Mark where platelets are.
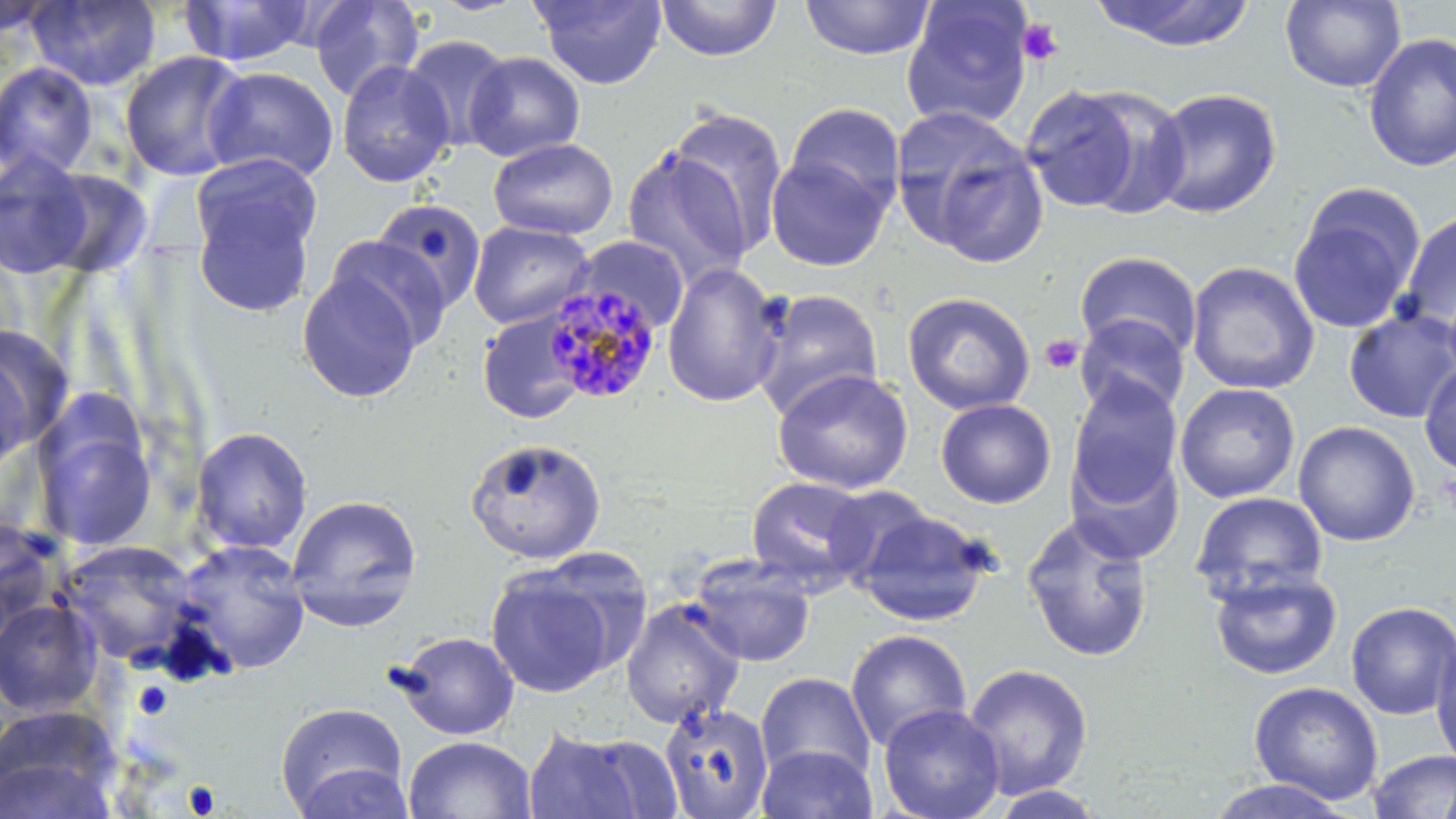

Approximate bounding boxes as (x1, y1, x2, y2) in pixels.
Platelets: (1017, 18, 1064, 66), (1039, 333, 1085, 375), (133, 681, 173, 720), (183, 781, 221, 817).

slide-level diagnosis = Plasmodium malariae
image size = 1456×819 pixels
uninfected red blood cell locations = approximate bounding boxes as (x1, y1, x2, y2) in pixels: (28, 0, 162, 92), (308, 0, 425, 102), (532, 0, 667, 90), (655, 0, 782, 62), (800, 0, 935, 60), (1091, 0, 1256, 51), (1280, 0, 1406, 93), (901, 1, 1035, 130), (0, 2, 56, 39), (178, 2, 315, 68), (1363, 32, 1456, 173), (402, 35, 514, 152), (119, 51, 252, 181), (463, 51, 585, 162), (336, 59, 455, 187), (0, 61, 99, 180), (203, 66, 340, 183), (1020, 85, 1157, 214), (1146, 87, 1282, 219), (783, 101, 907, 221), (890, 105, 1048, 266), (665, 106, 789, 257), (488, 137, 619, 240), (621, 146, 754, 288), (0, 150, 96, 279), (765, 153, 892, 271), (189, 160, 322, 316), (38, 168, 154, 278), (1289, 183, 1425, 335), (370, 198, 487, 314), (1399, 211, 1456, 334), (468, 220, 594, 330), (324, 235, 453, 352), (567, 235, 690, 336), (1074, 251, 1203, 363), (1185, 260, 1321, 395), (662, 262, 786, 407), (296, 268, 424, 403), (749, 288, 885, 420), (902, 291, 1036, 415), (1343, 308, 1456, 423), (477, 311, 588, 424), (1075, 314, 1190, 419), (0, 325, 64, 463), (0, 347, 35, 482), (1418, 360, 1456, 476), (772, 368, 914, 495), (1067, 376, 1182, 508), (1174, 382, 1301, 504), (935, 398, 1057, 508), (31, 411, 160, 551), (1293, 420, 1421, 546), (189, 425, 313, 555), (465, 437, 607, 563), (1066, 446, 1185, 566), (744, 475, 873, 594), (821, 483, 937, 591), (1189, 491, 1328, 605), (286, 494, 423, 632), (853, 507, 996, 627), (1020, 513, 1155, 663), (0, 519, 65, 641), (57, 539, 201, 667), (175, 539, 312, 675), (688, 555, 816, 667), (484, 559, 625, 699), (1208, 565, 1342, 680), (621, 598, 746, 729), (0, 599, 103, 717), (1345, 601, 1456, 720), (845, 628, 972, 753), (390, 631, 520, 740), (1430, 632, 1456, 770), (961, 662, 1094, 800), (755, 671, 876, 783), (1248, 680, 1385, 805), (275, 701, 409, 818), (659, 701, 775, 818), (879, 703, 1006, 819), (0, 705, 123, 818), (520, 727, 671, 819), (403, 734, 537, 819), (756, 744, 877, 818), (1366, 750, 1456, 819), (290, 762, 417, 818), (1201, 776, 1360, 818), (985, 784, 1112, 818)
preparation = thin blood smear
stain = May-Grünwald-Giemsa
field of view = single
modality = optical microscopy
magnification = 1000x
Plasmodium malariae-infected red blood cell locations = approximate bounding boxes as (x1, y1, x2, y2) in pixels: (540, 282, 662, 404)